Classify this cell by malaria status.
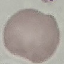

Uninfected.

capture = smartphone through the microscope eyepiece
stain = Giemsa
image type = automatically extracted cell patch, resized to 64 × 64 pixels
preparation = thin blood smear